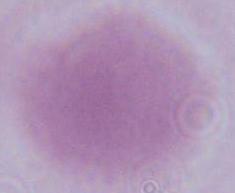

Summary:
  - Magnification: 1000x
  - Modality: photomicrograph
  - Identification: erythrocyte